Describe the morphology of the erythrocytes.
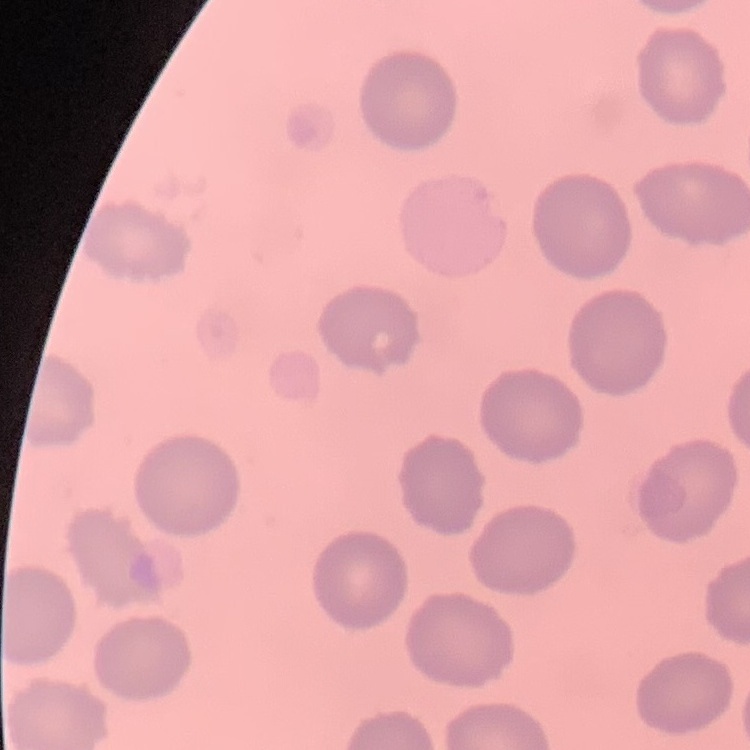
No rouleaux formation.

Summary:
  - Preparation: thin blood film
  - Image type: one tile cut from a larger photomicrograph
  - Stain: Field's or Giemsa